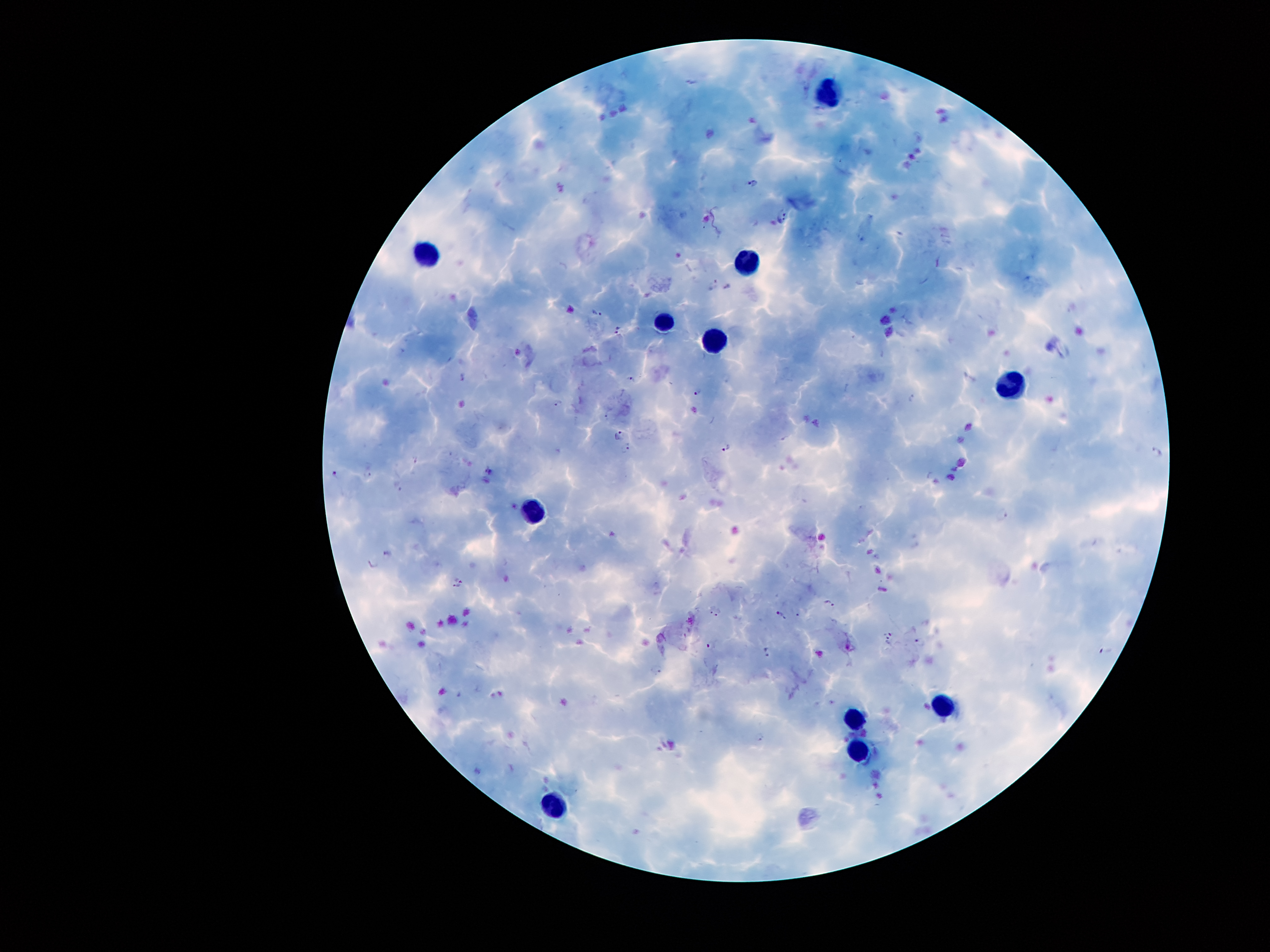 Approximate centers as {x, y} in pixels. Leukocyte locations: {828, 90}, {426, 252}, {748, 261}, {664, 322}, {712, 336}, {1008, 380}, {530, 511}, {946, 706}, {858, 723}, {859, 751}, {553, 801}. Malaria parasite locations: {754, 181}, {781, 215}, {713, 286}, {596, 314}, {618, 329}, {632, 377}, {463, 378}, {698, 391}, {911, 399}, {558, 402}, {607, 415}, {618, 434}, {625, 449}, {726, 449}, {1157, 451}, {369, 472}, {334, 473}, {398, 486}, {1003, 516}, {389, 554}, {373, 564}, {459, 578}, {457, 587}, {830, 603}, {712, 609}, {720, 612}, {780, 615}, {890, 634}, {920, 642}, {712, 645}, {768, 651}, {656, 669}, {762, 738}. 100x magnification. Patient malaria status: infected with Plasmodium falciparum. Thick blood smear. Photographed through the microscope eyepiece with a smartphone camera. One field from this slide. Image is 1270×952 pixels. Giemsa-stained preparation.